Assess the morphology of the erythrocytes.
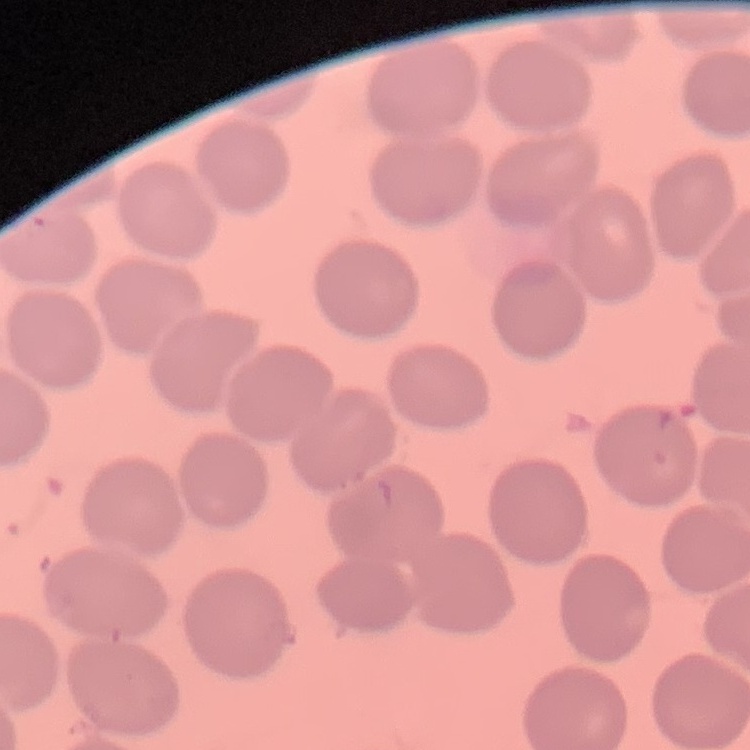
They show no rouleaux formation.

One tile cut from a larger photomicrograph. Thin peripheral smear. Stained with either Field's or Giemsa.